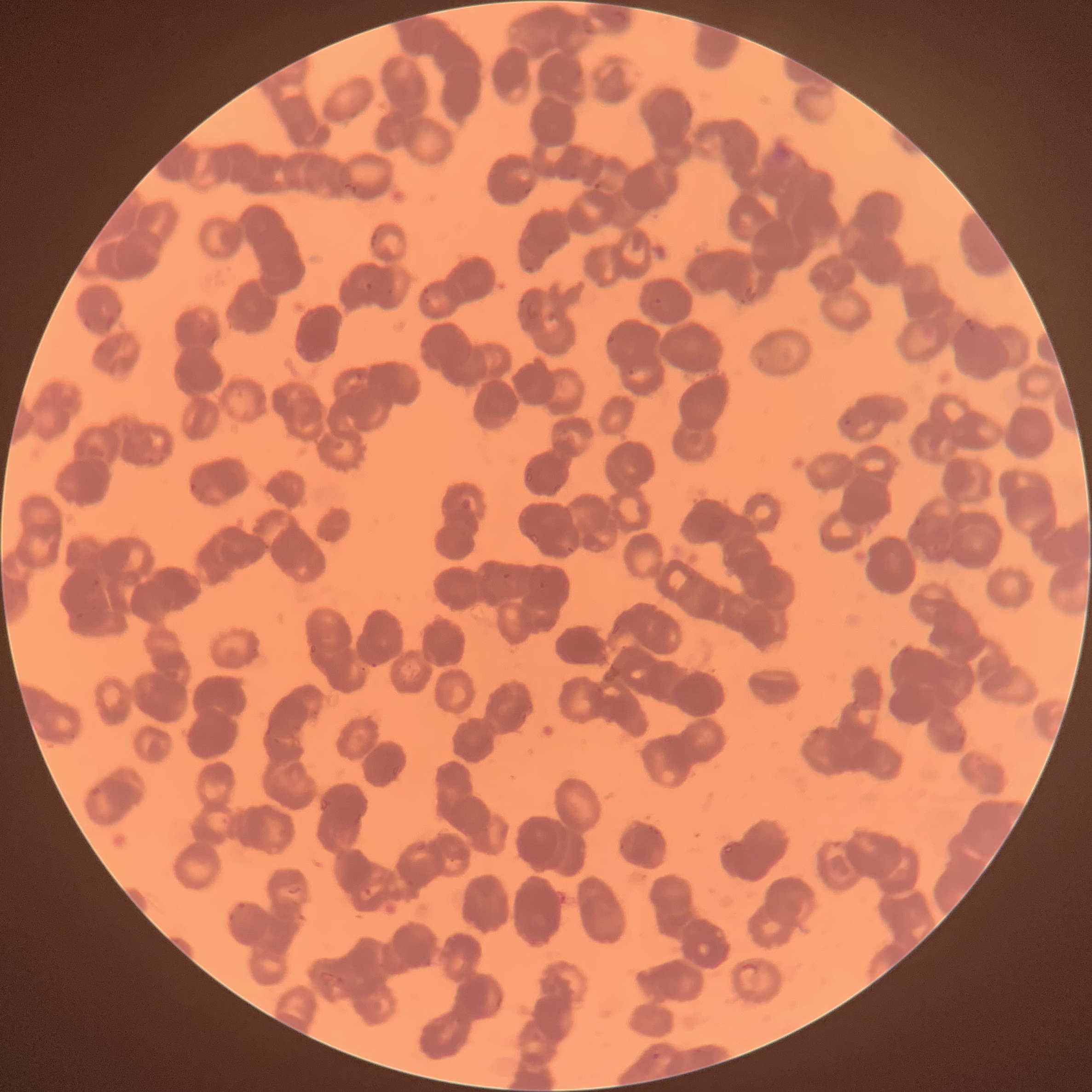

Summary:
  - Coordinate format: approximate bounding boxes as (x1, y1, x2, y2) in pixels
  - Plasmodium parasite locations: (592, 180, 603, 191), (547, 249, 555, 256), (523, 264, 536, 275), (365, 282, 374, 290), (421, 286, 431, 304), (387, 287, 396, 294), (650, 296, 662, 310), (965, 318, 972, 328), (607, 333, 617, 344), (628, 368, 641, 375), (355, 371, 364, 384), (843, 414, 855, 429), (145, 454, 165, 465), (911, 514, 924, 530), (563, 545, 576, 553), (502, 573, 512, 580), (370, 660, 379, 668), (520, 712, 529, 723), (89, 786, 103, 796), (363, 885, 372, 896), (227, 902, 244, 921), (335, 974, 346, 986), (649, 1050, 670, 1062)
  - Plasmodium parasites too small for a box (approximate centers as (x, y) in pixels): (652, 829)
  - Image size: 1092×1092 pixels
  - Preparation: thin blood film
  - Modality: light microscopy
  - Red blood cell morphology: rouleaux formation